Locate every blood parasite and identify its species.
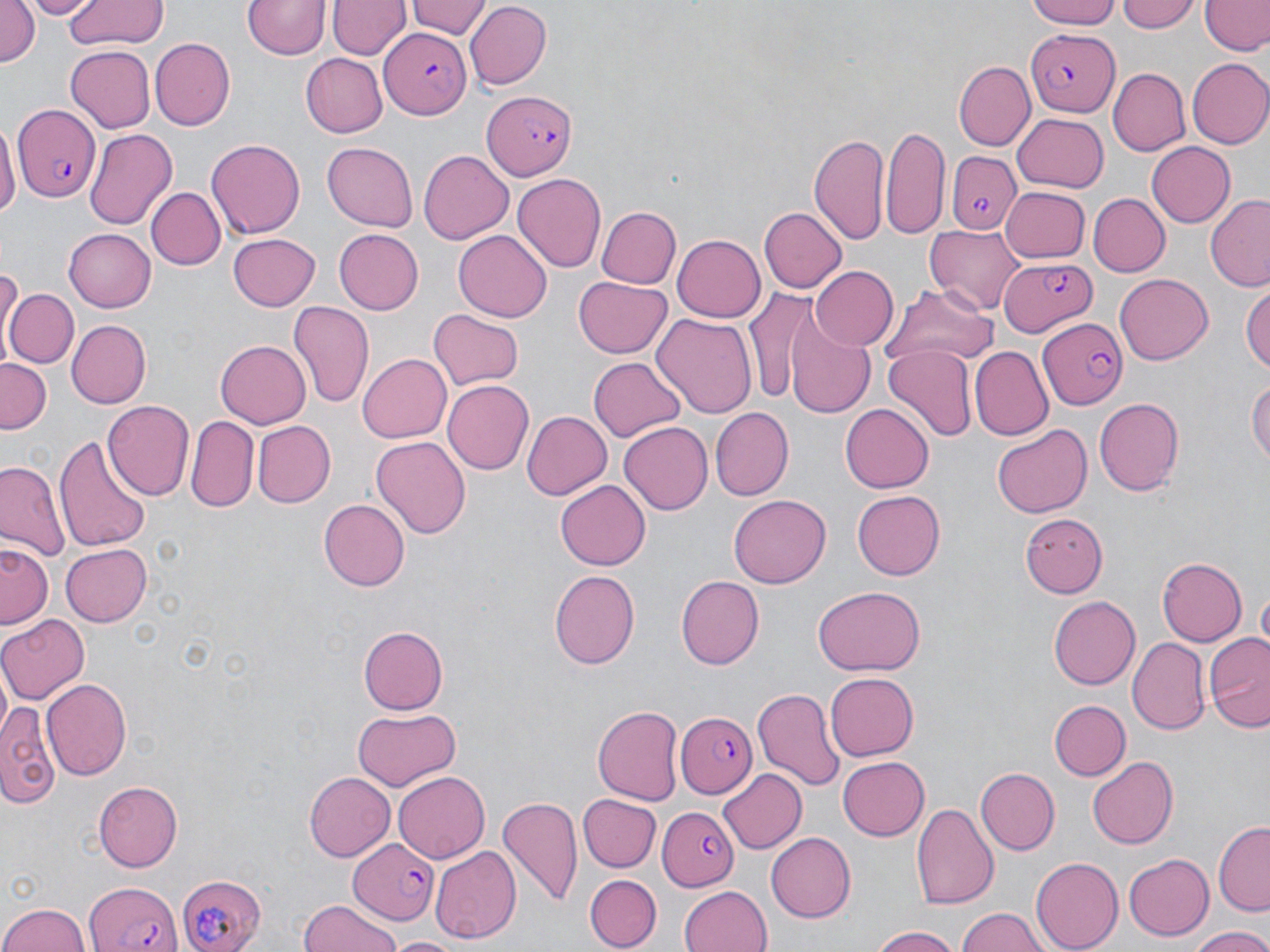

Approximate bounding boxes as named x1/y1/x2/y2 corners in pixels.
Plasmodium falciparum-infected red blood cells: (x1=379, y1=28, x2=471, y2=117), (x1=1025, y1=31, x2=1117, y2=116), (x1=483, y1=90, x2=576, y2=180), (x1=14, y1=107, x2=101, y2=200), (x1=945, y1=150, x2=1021, y2=234), (x1=997, y1=255, x2=1100, y2=335), (x1=1040, y1=319, x2=1128, y2=407), (x1=678, y1=712, x2=757, y2=798), (x1=658, y1=806, x2=739, y2=892), (x1=346, y1=837, x2=438, y2=924), (x1=175, y1=872, x2=266, y2=951), (x1=85, y1=878, x2=182, y2=952).
No Plasmodium ovale, Plasmodium malariae, Plasmodium vivax, Babesia divergens, or Trypanosoma brucei observed.

Summary:
  - Uninfected red blood cell locations: (x1=0, y1=0, x2=39, y2=71), (x1=28, y1=0, x2=90, y2=19), (x1=63, y1=0, x2=167, y2=48), (x1=242, y1=0, x2=332, y2=61), (x1=404, y1=0, x2=490, y2=39), (x1=1023, y1=0, x2=1126, y2=29), (x1=1119, y1=0, x2=1201, y2=32), (x1=329, y1=1, x2=409, y2=60), (x1=1202, y1=1, x2=1268, y2=57), (x1=465, y1=2, x2=552, y2=87), (x1=150, y1=38, x2=234, y2=131), (x1=65, y1=45, x2=156, y2=132), (x1=297, y1=52, x2=385, y2=137), (x1=1186, y1=58, x2=1270, y2=149), (x1=953, y1=60, x2=1034, y2=151), (x1=1106, y1=67, x2=1190, y2=155), (x1=1012, y1=113, x2=1108, y2=191), (x1=0, y1=118, x2=15, y2=223), (x1=881, y1=125, x2=950, y2=238), (x1=83, y1=128, x2=177, y2=231), (x1=809, y1=133, x2=890, y2=247), (x1=206, y1=138, x2=305, y2=238), (x1=1146, y1=142, x2=1235, y2=228), (x1=321, y1=143, x2=417, y2=231), (x1=419, y1=151, x2=513, y2=243), (x1=512, y1=173, x2=607, y2=272), (x1=147, y1=188, x2=225, y2=269), (x1=1000, y1=188, x2=1089, y2=263), (x1=1089, y1=194, x2=1170, y2=276), (x1=1205, y1=195, x2=1270, y2=291), (x1=597, y1=206, x2=682, y2=289), (x1=758, y1=207, x2=846, y2=292), (x1=925, y1=224, x2=1026, y2=314), (x1=64, y1=229, x2=157, y2=311), (x1=334, y1=230, x2=423, y2=314), (x1=454, y1=230, x2=551, y2=320), (x1=227, y1=233, x2=321, y2=311), (x1=673, y1=234, x2=767, y2=321), (x1=808, y1=264, x2=898, y2=351), (x1=1114, y1=274, x2=1214, y2=364), (x1=573, y1=275, x2=674, y2=360), (x1=1241, y1=281, x2=1270, y2=378), (x1=888, y1=285, x2=997, y2=370), (x1=745, y1=287, x2=832, y2=409), (x1=3, y1=288, x2=78, y2=369), (x1=288, y1=302, x2=374, y2=412), (x1=427, y1=309, x2=524, y2=392), (x1=652, y1=309, x2=757, y2=415), (x1=780, y1=311, x2=875, y2=418), (x1=66, y1=320, x2=148, y2=408), (x1=216, y1=340, x2=310, y2=428), (x1=883, y1=346, x2=977, y2=440), (x1=969, y1=347, x2=1053, y2=441), (x1=358, y1=351, x2=452, y2=441), (x1=0, y1=356, x2=52, y2=432), (x1=590, y1=356, x2=686, y2=442), (x1=1248, y1=375, x2=1269, y2=473), (x1=441, y1=380, x2=532, y2=475), (x1=1094, y1=397, x2=1186, y2=497), (x1=102, y1=400, x2=194, y2=502), (x1=839, y1=402, x2=934, y2=492), (x1=710, y1=407, x2=794, y2=500), (x1=520, y1=410, x2=612, y2=500), (x1=186, y1=415, x2=259, y2=511), (x1=252, y1=421, x2=334, y2=508), (x1=619, y1=422, x2=715, y2=515), (x1=991, y1=424, x2=1088, y2=519), (x1=55, y1=429, x2=150, y2=553), (x1=371, y1=436, x2=470, y2=542), (x1=1, y1=460, x2=69, y2=563), (x1=556, y1=482, x2=650, y2=569), (x1=851, y1=490, x2=943, y2=580), (x1=729, y1=495, x2=831, y2=588), (x1=320, y1=497, x2=409, y2=591), (x1=1018, y1=512, x2=1106, y2=595), (x1=1, y1=541, x2=52, y2=631), (x1=58, y1=543, x2=150, y2=628), (x1=1156, y1=557, x2=1247, y2=646), (x1=549, y1=568, x2=639, y2=668), (x1=676, y1=573, x2=765, y2=669), (x1=813, y1=587, x2=926, y2=678), (x1=1050, y1=594, x2=1141, y2=690), (x1=1, y1=615, x2=90, y2=706), (x1=358, y1=626, x2=448, y2=713), (x1=1203, y1=632, x2=1270, y2=731), (x1=1128, y1=637, x2=1210, y2=735), (x1=826, y1=673, x2=918, y2=760), (x1=42, y1=678, x2=130, y2=780), (x1=753, y1=685, x2=845, y2=793), (x1=1047, y1=700, x2=1129, y2=781), (x1=0, y1=703, x2=61, y2=806), (x1=593, y1=705, x2=683, y2=805), (x1=350, y1=708, x2=461, y2=788), (x1=838, y1=757, x2=930, y2=841), (x1=1088, y1=758, x2=1178, y2=848), (x1=719, y1=767, x2=807, y2=853), (x1=977, y1=768, x2=1059, y2=854), (x1=302, y1=770, x2=394, y2=861), (x1=390, y1=771, x2=489, y2=864), (x1=94, y1=779, x2=183, y2=869), (x1=498, y1=795, x2=583, y2=907), (x1=576, y1=795, x2=660, y2=872), (x1=912, y1=802, x2=999, y2=910), (x1=1214, y1=821, x2=1269, y2=914), (x1=767, y1=831, x2=856, y2=923), (x1=430, y1=844, x2=519, y2=942), (x1=1122, y1=853, x2=1214, y2=941), (x1=1030, y1=857, x2=1124, y2=951), (x1=585, y1=873, x2=662, y2=949), (x1=678, y1=884, x2=772, y2=952), (x1=296, y1=900, x2=404, y2=952), (x1=0, y1=902, x2=94, y2=952), (x1=958, y1=908, x2=1048, y2=952), (x1=869, y1=925, x2=965, y2=952), (x1=1188, y1=927, x2=1270, y2=952), (x1=390, y1=937, x2=462, y2=952)
  - Slide-level diagnosis: Plasmodium falciparum
  - Field of view: single
  - Preparation: thin blood smear
  - Stain: May-Grünwald-Giemsa
  - Modality: optical microscopy
  - Image size: 1270×952 pixels
  - Magnification: 1000x